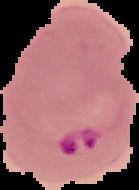

Summary:
  - Image type: segmented cell region with the area outside set to black
  - Preparation: thin blood film
  - Image size: 139×190 pixels
  - Result: malaria parasites identified